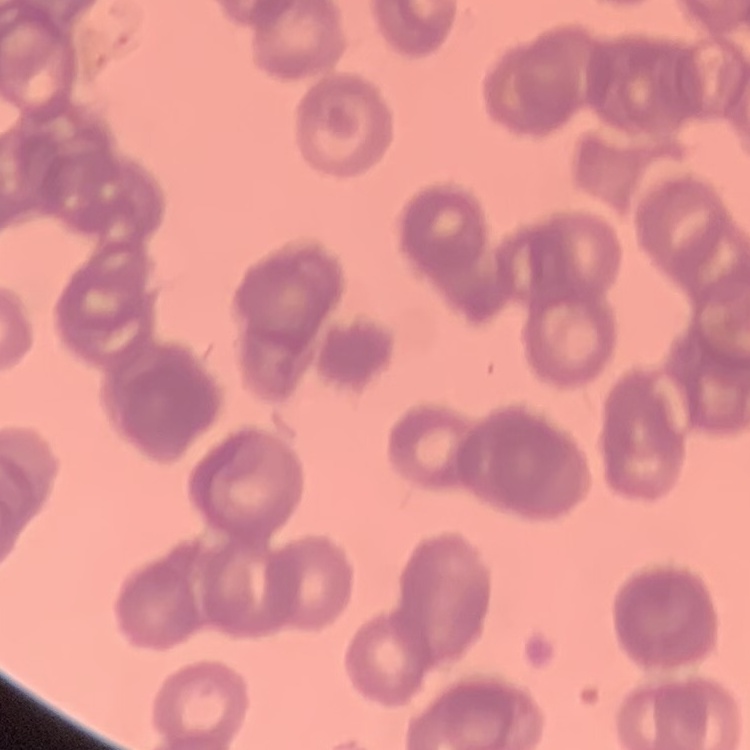

{
  "erythrocyte_morphology": "rouleaux formation",
  "stain": "Field's or Giemsa",
  "preparation": "thin peripheral smear",
  "image_type": "square crop of a larger photomicrograph"
}